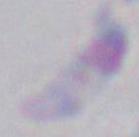
modality: photomicrograph
identification: Toxoplasma gondii
magnification: 1000x